Report the malaria status of this cell.
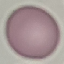

It is uninfected.

Summary:
  - Image type: cell patch, automatically extracted from a larger field of view and resized to 64 × 64 pixels
  - Capture: smartphone through the microscope eyepiece
  - Stain: Giemsa
  - Preparation: thin blood smear